State the preparation type.
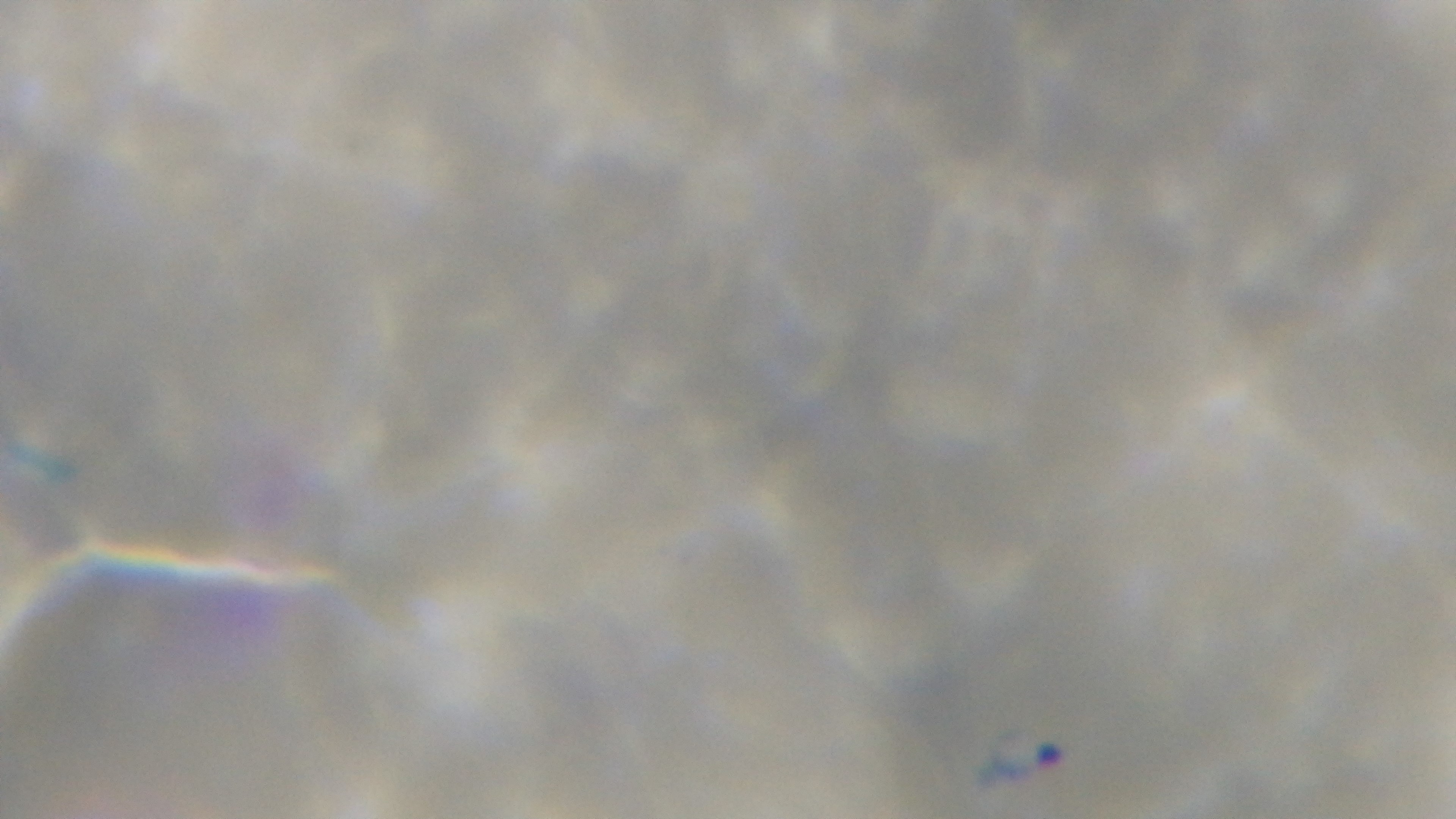

A thin smear.

Summary:
  - Malaria status: infected
  - Field of view: one from the slide
  - Modality: light microscopy
  - Capture: mounted 4K digital camera
  - Objective: 100x oil immersion
  - Stain: Giemsa